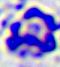
A white blood cell is shown. Captured at 400x magnification. Micrograph.